Identify the parasite.
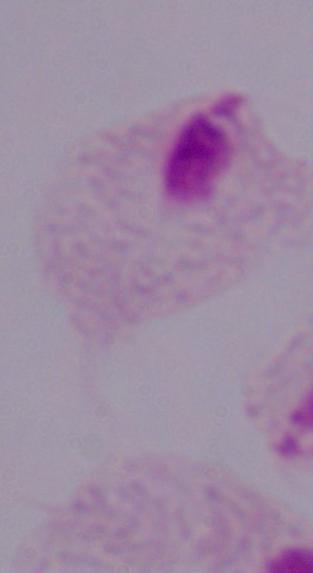
This is a trichomonad.

Captured at 1000x magnification. Micrograph.